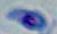

Summary:
  - Identification: Toxoplasma gondii
  - Magnification: 1000x
  - Modality: micrograph